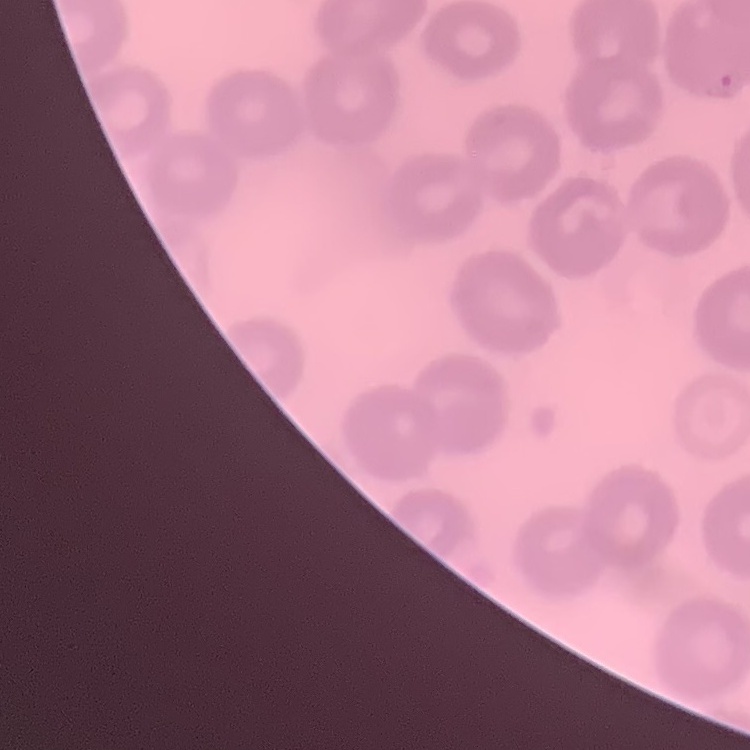
Summary:
  - Erythrocyte morphology: no rouleaux formation
  - Stain: Field's or Giemsa
  - Image type: square crop of a larger photomicrograph
  - Preparation: thin peripheral smear